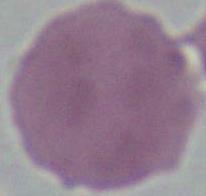
Summary:
  - Magnification: 1000x
  - Identification: erythrocyte
  - Modality: photomicrograph